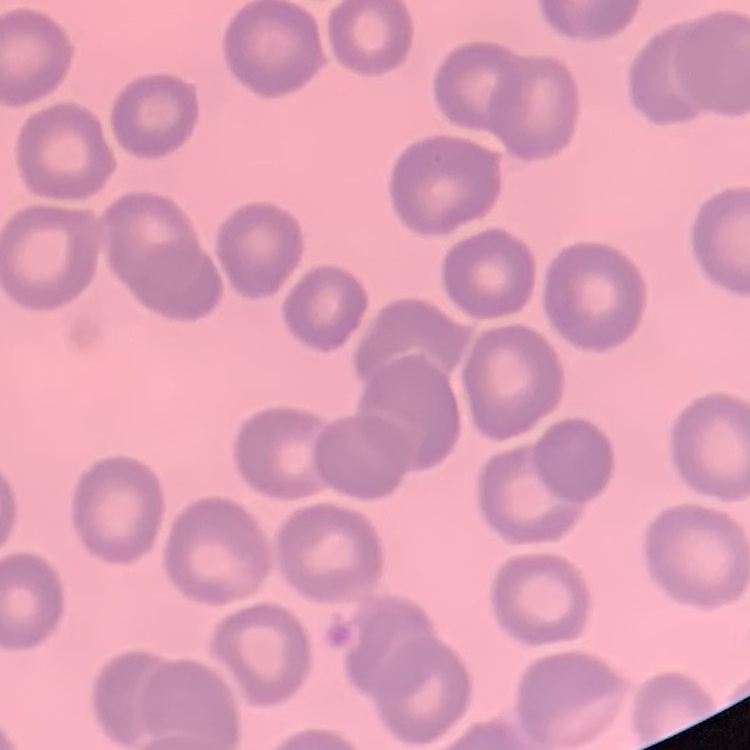

erythrocyte morphology = no rouleaux formation
preparation = thin blood film
image type = square crop of a larger photomicrograph
stain = Field's or Giemsa